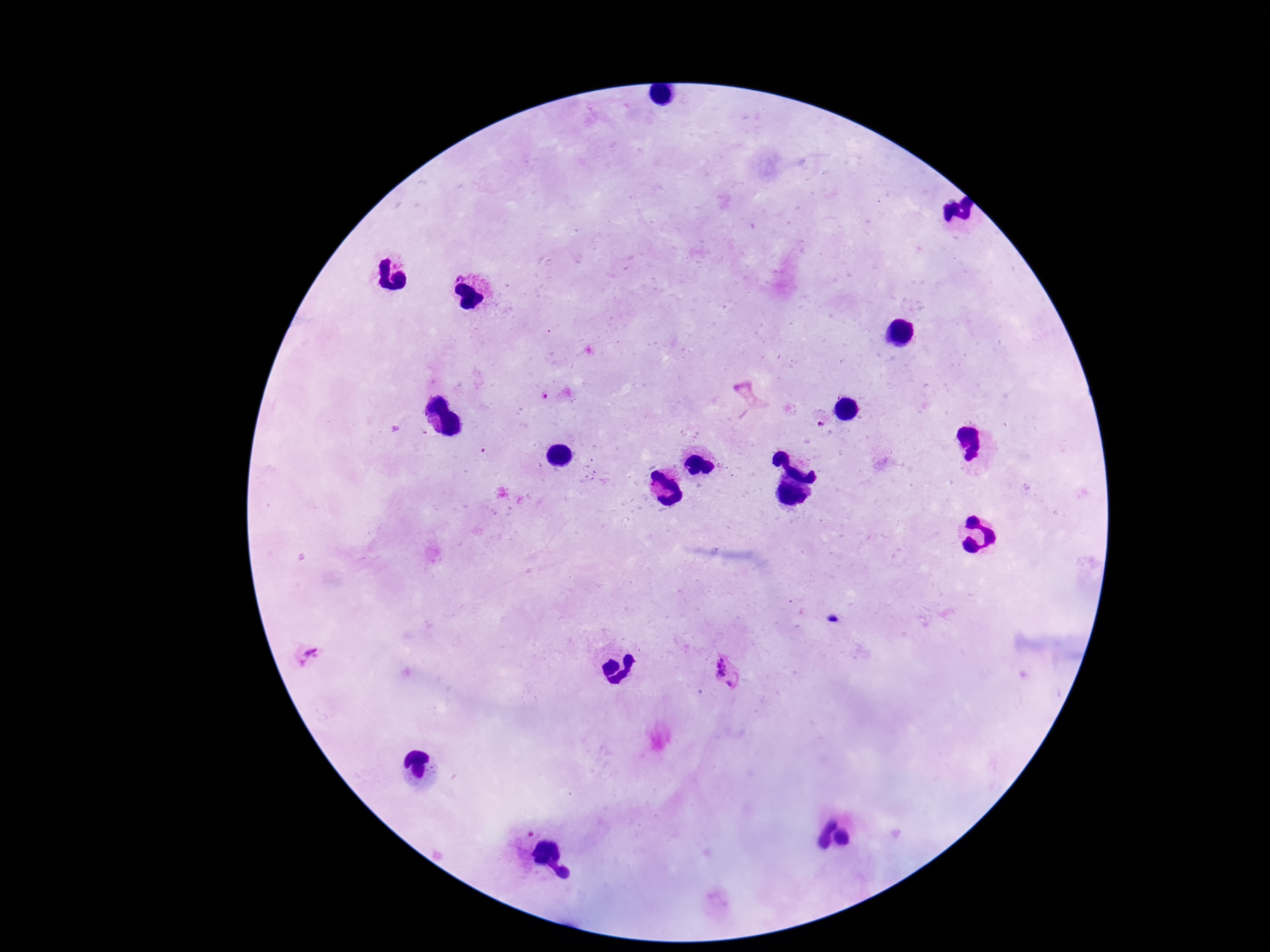

preparation = thick blood film
Plasmodium parasite locations = approximate centers as {x, y} in pixels: {544, 396}, {753, 397}, {821, 425}, {311, 657}, {725, 673}
patient malaria status = infected
stain = Giemsa
field of view = one from this slide
capture = smartphone camera through the microscope eyepiece
image size = 1270×952 pixels
magnification = 100x